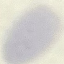

result: negative for malaria parasites
image_type: cell patch, automatically extracted from a larger field of view and resized to 64 × 64 pixels
preparation: thin blood film
stain: Giemsa
capture: smartphone through the microscope eyepiece